Locate every uninfected red blood cell.
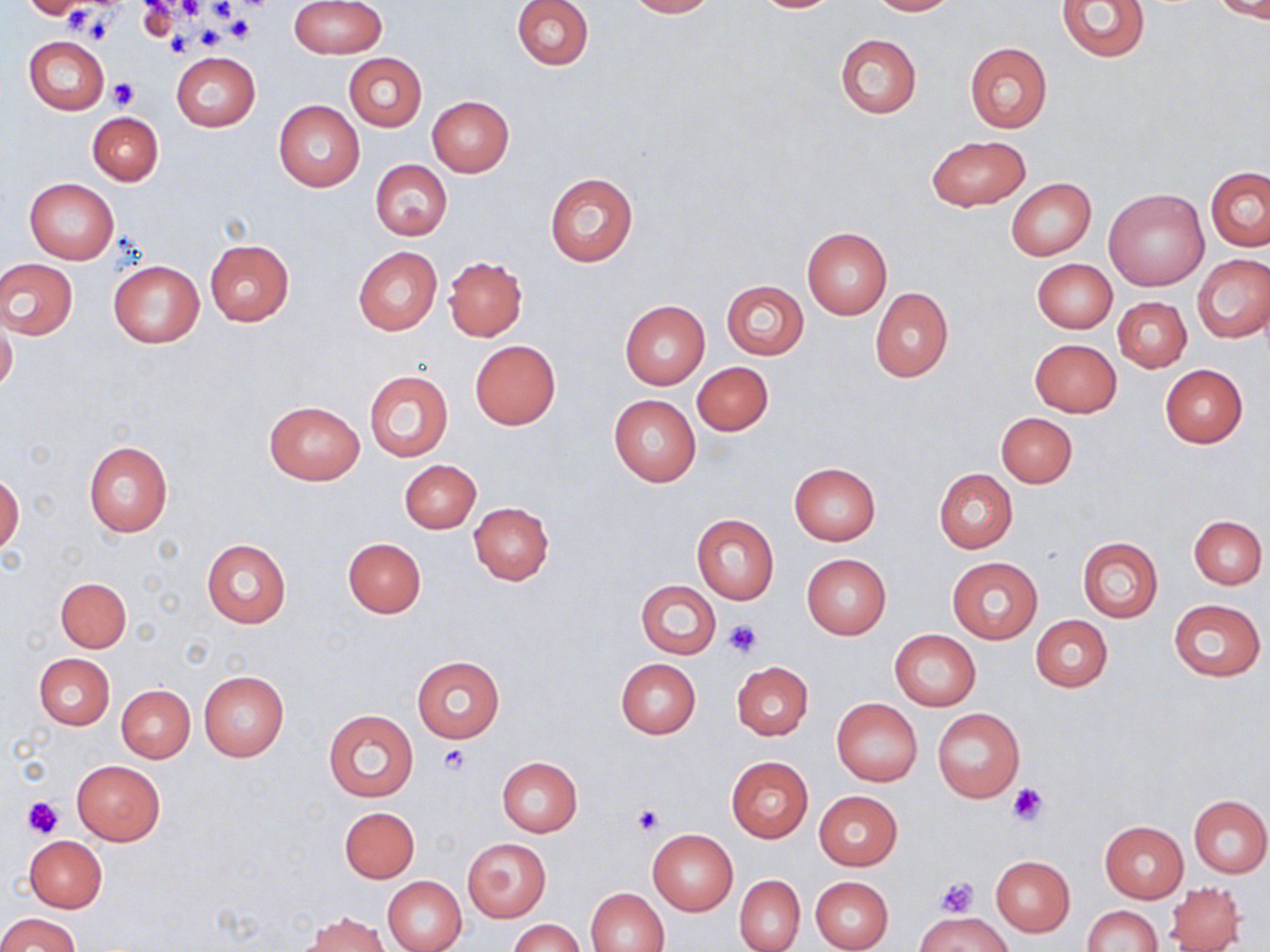

Approximate bounding boxes as (x1, y1, x2, y2) in pixels.
Uninfected red blood cells: (291, 0, 385, 58), (511, 0, 593, 71), (625, 0, 715, 18), (749, 0, 841, 13), (865, 0, 959, 15), (1056, 0, 1151, 61), (1212, 0, 1270, 22), (23, 1, 92, 19), (834, 32, 922, 118), (25, 35, 109, 115), (963, 42, 1054, 133), (171, 52, 260, 132), (343, 52, 426, 131), (427, 96, 514, 176), (274, 101, 364, 192), (86, 113, 163, 185), (927, 135, 1030, 211), (370, 160, 452, 241), (1205, 167, 1270, 251), (545, 172, 638, 266), (25, 178, 118, 263), (1007, 178, 1095, 261), (1104, 188, 1209, 290), (801, 227, 891, 319), (204, 239, 295, 325), (353, 246, 441, 334), (1194, 254, 1270, 342), (445, 256, 528, 341), (0, 258, 78, 340), (1033, 259, 1117, 332), (109, 261, 203, 347), (722, 280, 808, 359), (869, 289, 953, 383), (1113, 296, 1191, 373), (619, 301, 710, 389), (0, 318, 18, 395), (1029, 338, 1122, 417), (470, 340, 560, 429), (693, 362, 773, 436), (1160, 365, 1248, 448), (364, 369, 454, 463), (609, 395, 701, 487), (264, 400, 365, 485), (996, 412, 1077, 487), (82, 441, 173, 536), (399, 459, 480, 533), (789, 462, 880, 545), (934, 469, 1017, 552), (0, 474, 24, 555), (470, 502, 554, 584), (692, 514, 778, 604), (1189, 515, 1266, 588), (1078, 536, 1163, 622), (201, 537, 292, 628), (343, 537, 426, 617), (802, 554, 891, 639), (947, 558, 1042, 643), (55, 577, 131, 652), (636, 580, 721, 658), (1167, 598, 1266, 682), (1031, 615, 1111, 692), (890, 629, 981, 710), (34, 654, 113, 730), (413, 656, 504, 742), (615, 658, 701, 738), (732, 661, 813, 739), (198, 670, 287, 761), (116, 684, 195, 762), (831, 698, 922, 786), (932, 708, 1025, 802), (323, 709, 419, 802), (726, 756, 813, 842), (497, 757, 582, 837), (72, 760, 165, 845), (814, 791, 902, 870), (1188, 794, 1270, 877), (340, 807, 419, 882), (1099, 820, 1188, 903), (648, 829, 739, 916), (25, 836, 107, 912), (462, 837, 552, 922), (990, 855, 1075, 936), (734, 875, 805, 951), (383, 876, 466, 952), (811, 876, 893, 951), (1167, 882, 1246, 951), (585, 887, 669, 952), (1082, 905, 1160, 952), (915, 912, 1012, 952), (0, 913, 82, 952), (305, 914, 390, 952), (509, 918, 583, 952).

Platelet locations: (172, 0, 212, 20), (138, 3, 177, 38), (69, 7, 120, 42), (226, 14, 256, 43), (192, 23, 227, 50), (165, 33, 191, 57), (109, 79, 139, 108), (721, 618, 765, 659), (440, 744, 471, 772), (1005, 782, 1049, 824), (21, 796, 64, 838), (631, 804, 664, 836), (934, 876, 980, 917). Slide-level diagnosis: negative for blood parasites. Single field of view. Thin blood smear. Captured at 1000x magnification. Image is 1270×952 pixels. May-Grünwald-Giemsa-stained preparation. Light microscopy.